State the blood parasite species.
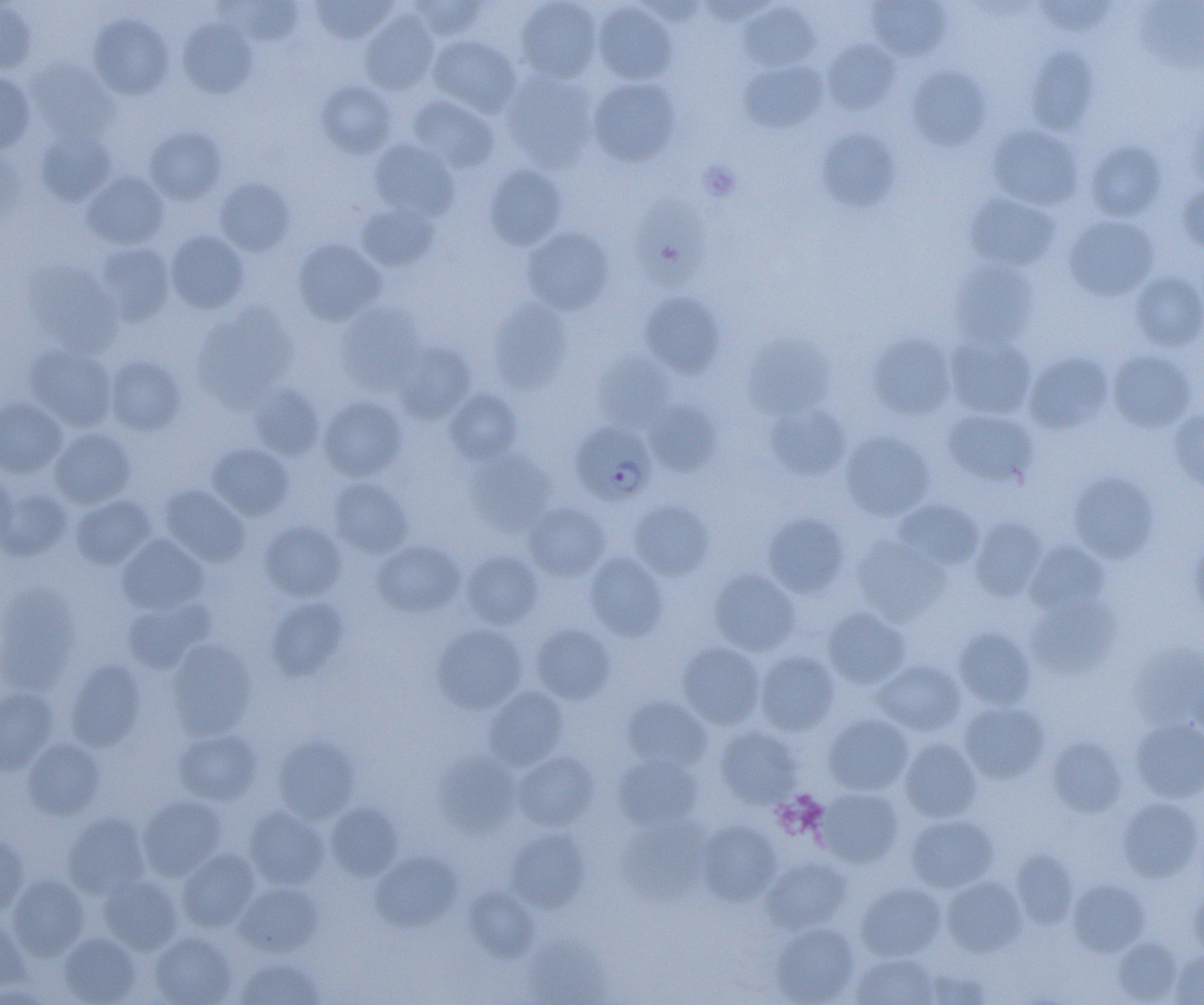
Plasmodium falciparum.

Summary:
  - Coordinate format: approximate bounding boxes as (x1, y1, x2, y2) in pixels
  - Uninfected red blood cell locations: (310, 0, 397, 43), (408, 0, 490, 41), (1033, 0, 1117, 37), (0, 1, 36, 75), (218, 1, 304, 44), (514, 1, 602, 83), (867, 1, 952, 62), (1137, 1, 1204, 73), (592, 2, 677, 85), (739, 2, 820, 71), (359, 11, 439, 95), (88, 13, 173, 100), (178, 19, 257, 99), (427, 35, 521, 117), (822, 38, 901, 115), (1025, 47, 1098, 136), (25, 59, 117, 144), (740, 60, 828, 133), (906, 64, 992, 150), (502, 70, 599, 171), (0, 72, 36, 153), (589, 77, 681, 167), (316, 79, 397, 158), (406, 95, 499, 173), (1184, 109, 1204, 194), (987, 124, 1084, 210), (145, 126, 227, 204), (35, 128, 116, 205), (817, 128, 900, 213), (369, 139, 459, 220), (1083, 140, 1167, 221), (0, 147, 27, 228), (484, 164, 567, 250), (82, 171, 169, 250), (214, 177, 295, 256), (1177, 182, 1204, 258), (634, 194, 711, 291), (964, 194, 1060, 270), (356, 202, 441, 270), (1063, 214, 1159, 301), (522, 226, 613, 314), (165, 230, 249, 314), (293, 239, 386, 326), (94, 242, 175, 326), (948, 260, 1038, 349), (24, 261, 123, 355), (1131, 271, 1204, 351), (639, 292, 724, 378), (487, 300, 571, 393), (337, 302, 428, 395), (193, 303, 298, 409), (867, 331, 956, 420), (743, 333, 837, 419), (945, 334, 1037, 419), (395, 342, 477, 424), (25, 343, 117, 431), (1107, 350, 1196, 432), (1024, 351, 1113, 435), (592, 352, 675, 430), (105, 355, 186, 436), (248, 383, 325, 460), (444, 388, 522, 465), (319, 395, 407, 481), (0, 396, 67, 478), (645, 399, 722, 476), (764, 401, 851, 480), (941, 409, 1038, 487), (1169, 409, 1204, 492), (50, 427, 136, 508), (840, 431, 935, 520), (207, 442, 294, 520), (465, 451, 556, 535), (0, 470, 18, 551), (1070, 471, 1158, 562), (329, 478, 413, 558), (158, 484, 250, 566), (0, 485, 72, 561), (71, 494, 157, 568), (628, 499, 715, 580), (894, 499, 984, 570), (526, 501, 610, 581), (763, 513, 849, 597), (970, 516, 1047, 601), (259, 521, 346, 601), (117, 534, 208, 614), (850, 535, 949, 625), (1190, 535, 1204, 619), (372, 540, 464, 616), (1026, 541, 1110, 617), (460, 550, 543, 629), (584, 552, 668, 641), (709, 569, 800, 655), (0, 584, 80, 692), (1026, 596, 1120, 679), (266, 597, 349, 680), (122, 598, 214, 673), (822, 607, 911, 688), (531, 623, 615, 704), (432, 624, 527, 713), (954, 626, 1036, 709), (167, 640, 256, 738), (677, 642, 765, 729), (1128, 643, 1204, 730), (755, 650, 840, 735), (65, 659, 146, 751), (874, 660, 965, 737), (0, 687, 59, 774), (484, 687, 568, 769), (621, 695, 712, 772), (959, 702, 1049, 783), (823, 713, 914, 794), (1131, 717, 1204, 802), (714, 726, 801, 809), (174, 728, 263, 805), (273, 734, 359, 823), (899, 736, 982, 822), (1047, 736, 1127, 818), (23, 737, 105, 819), (513, 751, 598, 831), (434, 752, 521, 837), (614, 754, 703, 830), (814, 787, 903, 869), (138, 795, 226, 880), (1118, 797, 1203, 881), (325, 802, 403, 881), (244, 806, 329, 889), (62, 813, 150, 898), (905, 814, 998, 893), (618, 818, 709, 904), (696, 820, 782, 906), (507, 829, 591, 912), (0, 836, 29, 916), (177, 848, 260, 931), (371, 849, 462, 931), (1010, 849, 1079, 929), (761, 856, 851, 933), (8, 873, 90, 960), (99, 874, 182, 954), (941, 876, 1026, 956), (1067, 880, 1149, 957), (235, 882, 323, 956), (855, 882, 947, 961), (463, 887, 539, 962), (1190, 888, 1204, 959), (0, 915, 29, 994), (770, 922, 859, 1005), (59, 932, 142, 1004), (150, 932, 237, 1005), (521, 933, 612, 1004), (1111, 937, 1182, 1003), (1169, 950, 1204, 1005), (850, 953, 940, 1004), (235, 957, 324, 1004), (919, 965, 991, 1004)
  - Plasmodium falciparum-infected red blood cell locations: (566, 418, 651, 504)
  - Platelet locations: (699, 161, 741, 202)
  - Field of view: one of a larger specimen
  - Magnification: 1000x
  - Modality: optical microscopy
  - Preparation: thin blood smear
  - Image size: 1204×1005 pixels